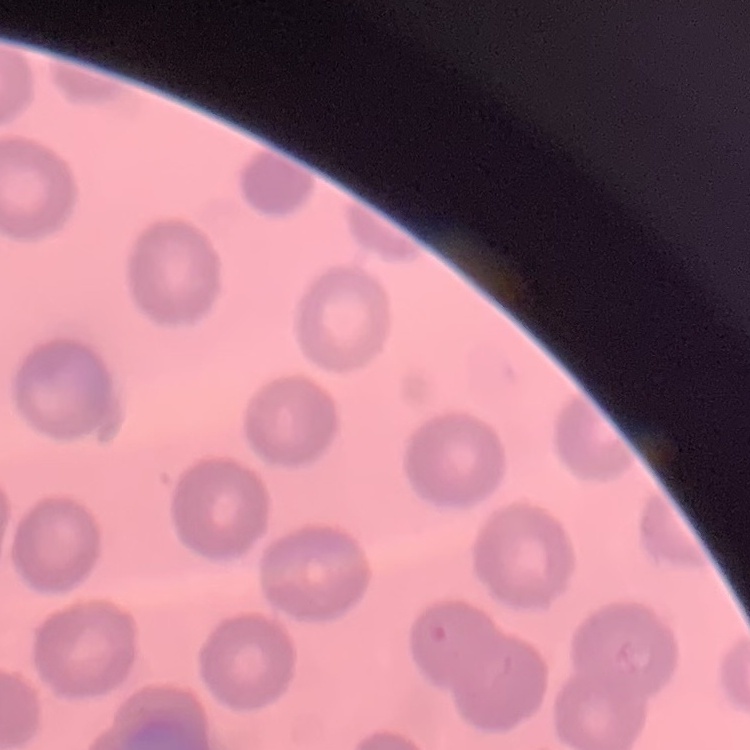

Summary:
  - Erythrocyte morphology: no rouleaux formation
  - Preparation: thin peripheral smear
  - Stain: Field's or Giemsa
  - Image type: square crop of a larger photomicrograph